Assess this cell for malaria.
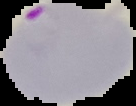

Parasitized.

Summary:
  - Image type: cell region segmented out of the field of view; surrounding area masked to black
  - Preparation: thin blood smear
  - Image size: 136×106 pixels